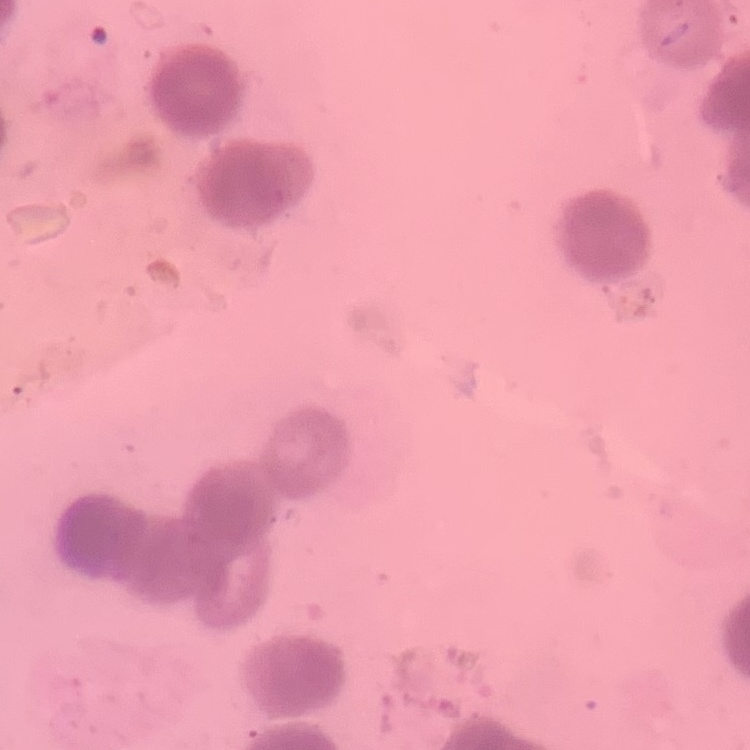

Summary:
  - Red blood cell morphology: rouleaux formation
  - Stain: Field's or Giemsa
  - Image type: one tile cut from a larger photomicrograph
  - Preparation: thin blood film